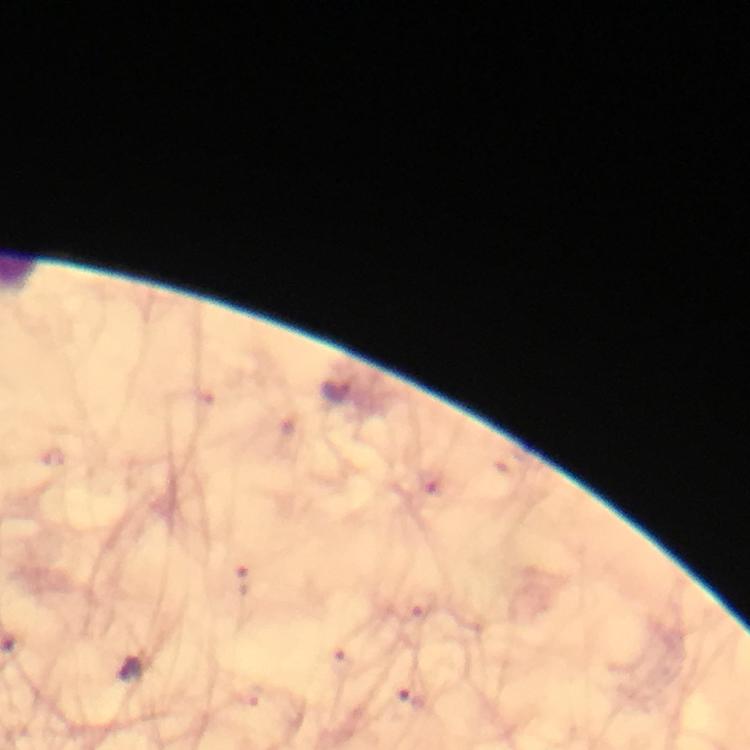

Approximate centers as {x, y} in pixels.
Summary:
  - Malaria parasite locations: {242, 580}, {128, 669}, {412, 697}
  - Magnification: 100x
  - Cropped from: one field of view
  - Image size: 750×750 pixels
  - Stain: Giemsa
  - Preparation: thick blood film
  - Capture: smartphone camera through the microscope
  - Context: from a diagnostic examination for malaria
  - Immersion oil: applied